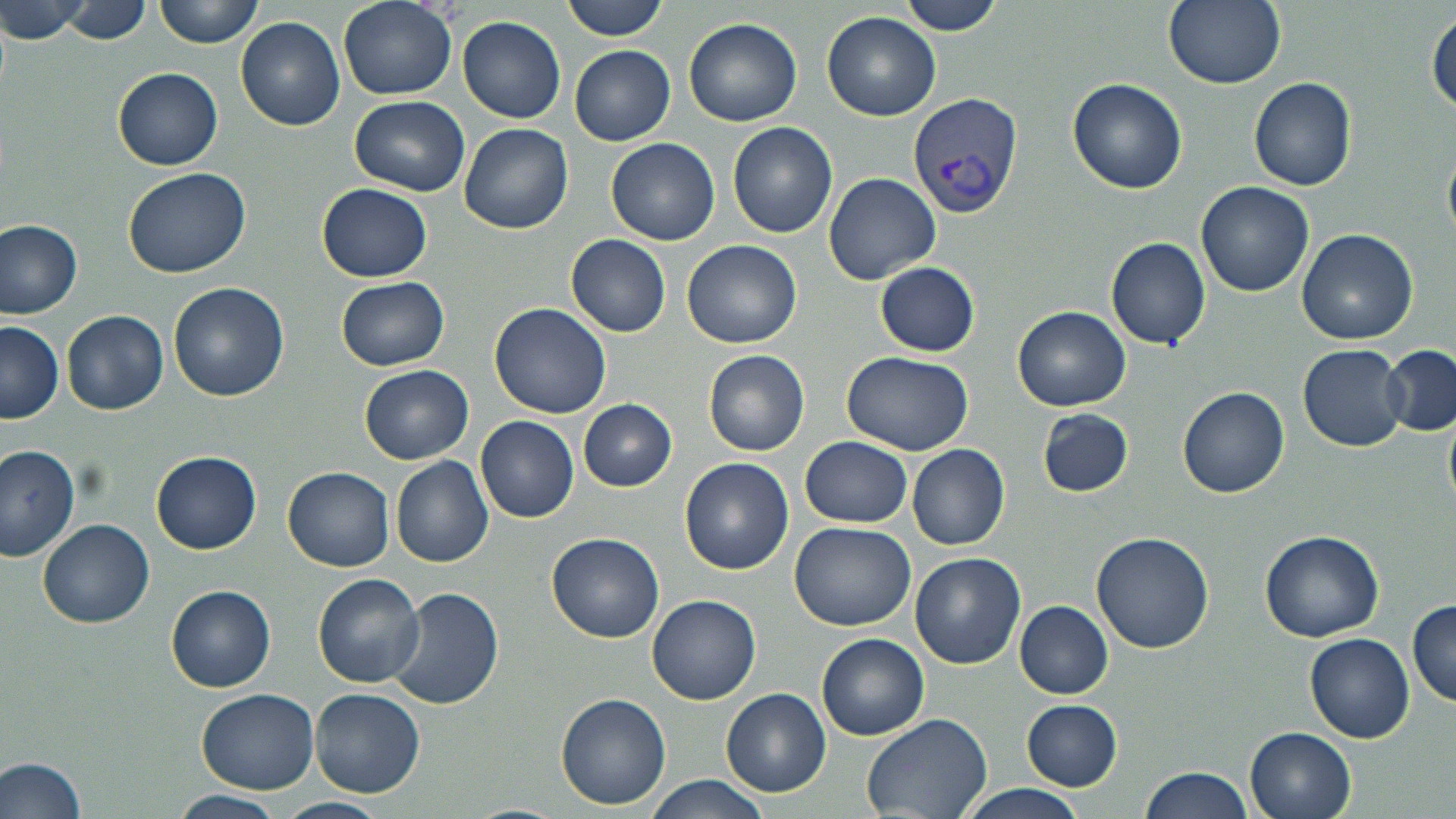

{
  "slide_level_diagnosis": "Plasmodium vivax",
  "modality": "optical microscopy",
  "field_of_view": "single",
  "image_size": "1456×819 pixels",
  "stain": "May-Grünwald-Giemsa",
  "preparation": "thin blood smear",
  "uninfected_red_blood_cell_locations": "approximate bounding boxes as (x1,y1)-(x2,y2) corner pairs in pixels: (0,0)-(92,48), (154,0)-(264,47), (338,0)-(458,100), (560,0)-(669,39), (901,0)-(1008,35), (1162,0)-(1286,89), (60,1)-(151,43), (823,12)-(942,122), (1428,12)-(1455,116), (237,16)-(346,130), (682,16)-(802,127), (459,17)-(567,123), (570,45)-(675,145), (114,68)-(224,169), (1249,76)-(1357,190), (1068,77)-(1188,193), (349,96)-(468,194), (727,121)-(839,239), (460,124)-(574,234), (608,137)-(719,246), (123,166)-(251,277), (822,172)-(941,284), (1196,180)-(1315,296), (317,183)-(432,282), (0,219)-(82,319), (1297,229)-(1418,345), (567,234)-(671,338), (1106,237)-(1211,350), (682,239)-(802,349), (875,261)-(979,355), (336,275)-(450,371), (169,282)-(289,401), (489,302)-(611,419), (1014,305)-(1131,411), (63,310)-(169,415), (0,321)-(63,422), (1299,344)-(1407,451), (1380,345)-(1456,435), (703,349)-(810,456), (840,350)-(975,455), (359,362)-(472,464), (1179,387)-(1289,498), (578,399)-(677,491), (1036,408)-(1135,498), (475,413)-(579,523), (800,437)-(913,528), (907,442)-(1009,551), (0,444)-(81,560), (152,451)-(261,553), (391,457)-(494,567), (679,457)-(794,573), (284,467)-(394,570), (39,518)-(155,628), (790,521)-(915,631), (1260,529)-(1385,641), (546,532)-(665,642), (1091,532)-(1215,653), (910,553)-(1026,668), (312,573)-(425,688), (167,585)-(276,692), (389,588)-(503,713), (648,595)-(761,704), (1407,599)-(1456,707), (1016,602)-(1112,698), (1305,633)-(1415,742), (818,634)-(928,741), (310,687)-(425,798), (197,688)-(320,795), (721,689)-(830,796), (555,691)-(670,809), (1020,698)-(1124,790), (861,712)-(993,819), (1245,727)-(1357,819), (0,755)-(91,819), (1138,767)-(1254,819), (645,777)-(769,817), (950,783)-(1093,819), (171,790)-(285,817), (275,796)-(388,819)",
  "magnification": "1000x",
  "plasmodium_vivax_infected_red_blood_cell_locations": "approximate bounding boxes as (x1,y1)-(x2,y2) corner pairs in pixels: (908,93)-(1022,219)"
}